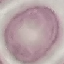

malaria_status: uninfected
capture: smartphone camera at the microscope eyepiece
image_type: cell patch, automatically extracted from a larger field of view and resized to 64 × 64 pixels
stain: Giemsa
preparation: thin smear